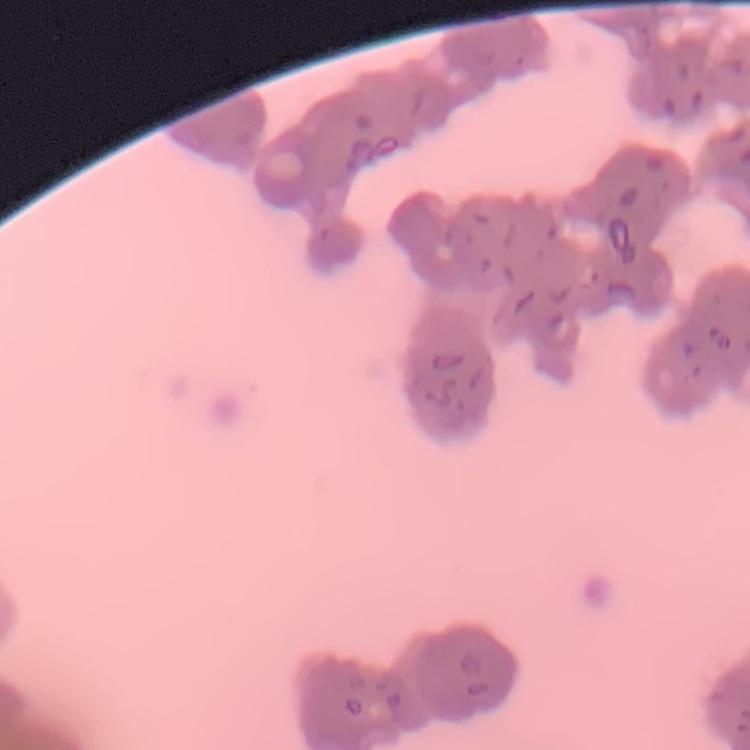
The red blood cells show rouleaux formation. Square crop of a larger photomicrograph. Thin blood smear. Stained with either Field's or Giemsa.